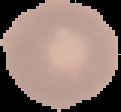
Summary:
  - Preparation: thin blood film
  - Image type: cell region segmented out of the field of view; surrounding area masked to black
  - Result: negative for Plasmodium parasites
  - Image size: 121×112 pixels